Give the position of every malaria parasite.
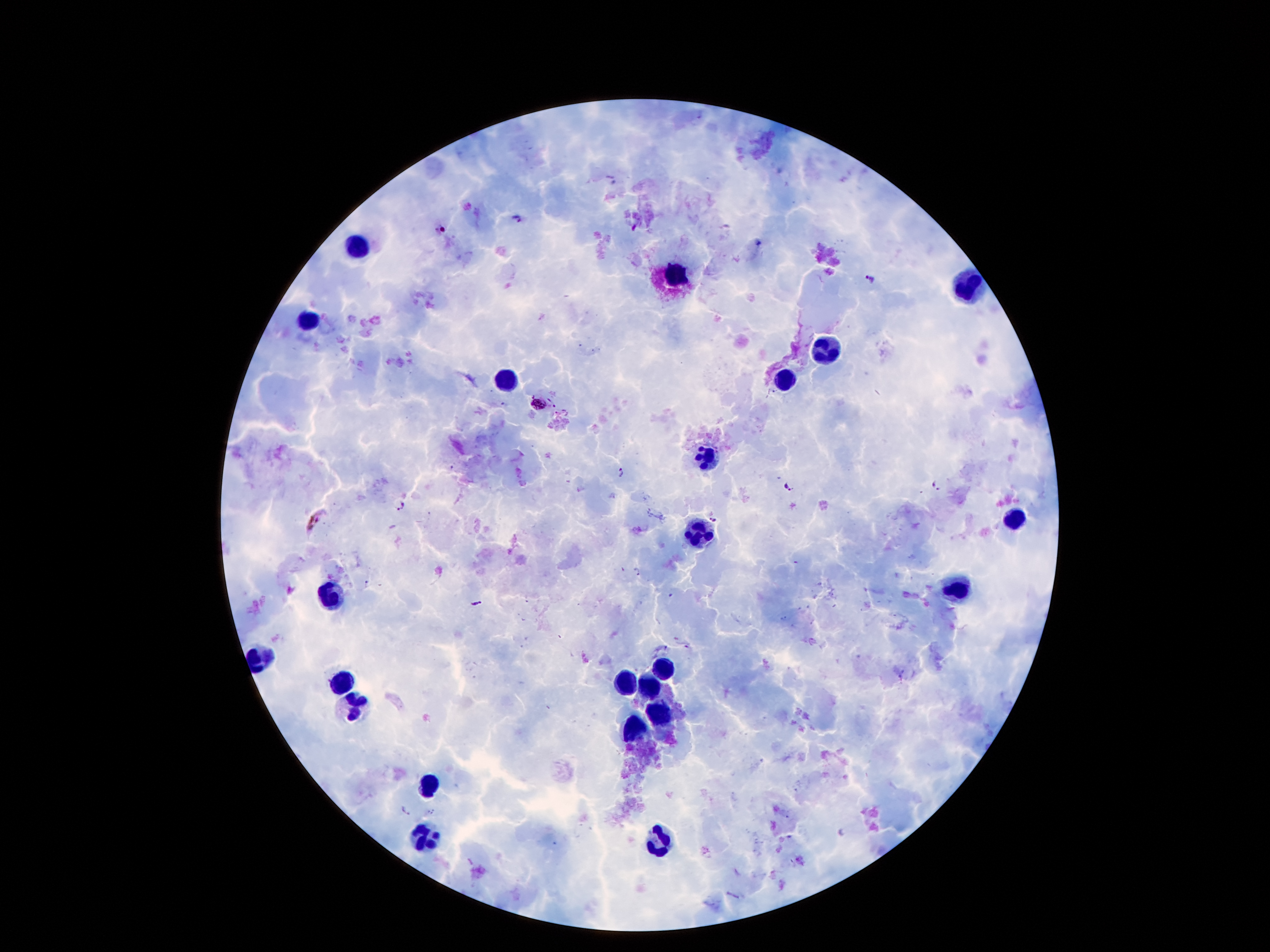

Approximate centers as (x, y) in pixels.
Malaria parasites: (518, 218), (635, 227), (441, 228), (758, 242), (868, 278), (540, 404), (620, 473), (789, 485), (936, 486), (401, 504), (714, 518), (313, 521), (636, 571), (367, 582), (478, 604), (407, 811).

Summary:
  - Leukocyte locations: (356, 247), (673, 274), (967, 287), (310, 319), (824, 348), (782, 380), (508, 381), (708, 456), (1017, 520), (696, 529), (958, 590), (332, 599), (258, 658), (661, 667), (626, 678), (341, 681), (647, 683), (357, 706), (659, 714), (633, 727), (427, 783), (425, 835), (666, 844)
  - Image size: 1270×952 pixels
  - Capture: smartphone camera through the microscope eyepiece
  - Magnification: 100x
  - Field of view: one from this slide
  - Stain: Giemsa
  - Patient malaria status: positive for Plasmodium falciparum
  - Preparation: thick blood smear